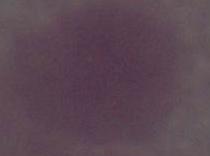
magnification: 1000x
identification: red blood cell
modality: photomicrograph